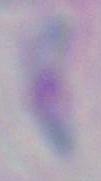

Toxoplasma gondii is seen. Micrograph. 1000x magnification.